Comment on the morphology of the red blood cells.
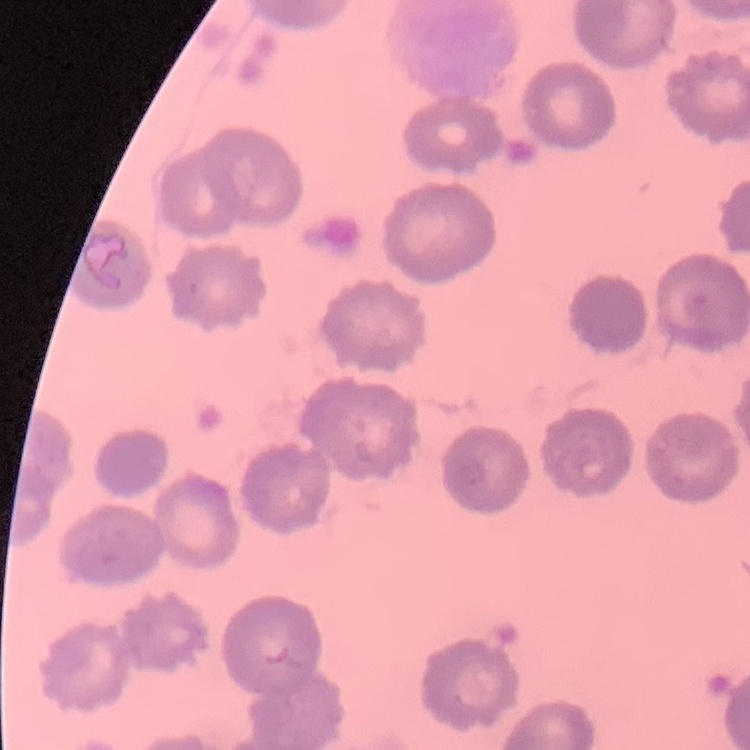

They show no rouleaux formation.

stain = Field's or Giemsa
image type = square crop of a larger photomicrograph
preparation = thin blood smear